Assess this cell for malaria.
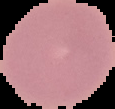
It is uninfected.

Summary:
  - Image type: segmented cell region with the area outside set to black
  - Preparation: thin blood smear
  - Image size: 115×109 pixels